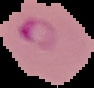
image type = segmented cell region on a black background
malaria status = parasitized
preparation = thin blood smear
image size = 94×88 pixels